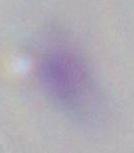
Summary:
  - Modality: micrograph
  - Magnification: 1000x
  - Identification: Toxoplasma gondii